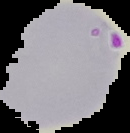

image_type: segmented cell region on a black background
image_size: 130×133 pixels
malaria_status: parasitized
preparation: thin blood film